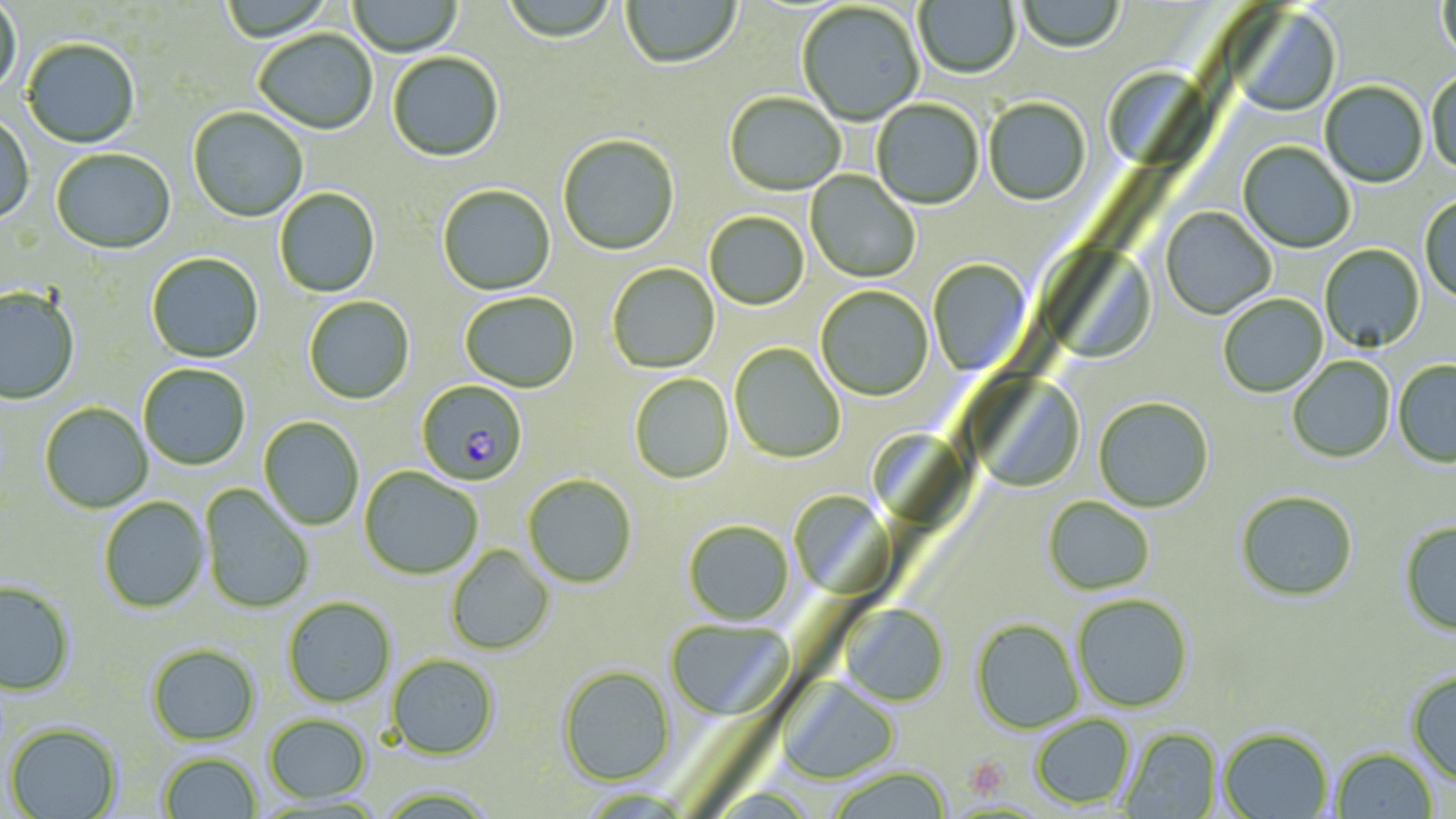

Summary:
  - Coordinate format: approximate bounding boxes as (x1,y1)-(x2,y2) corner pairs in pixels
  - Plasmodium falciparum-infected red blood cell locations: (415,380)-(528,487)
  - Uninfected red blood cell locations: (219,0)-(336,44), (500,0)-(619,46), (621,0)-(742,72), (914,0)-(1020,80), (1017,0)-(1124,54), (1438,0)-(1456,65), (0,1)-(21,101), (347,1)-(463,58), (797,4)-(924,127), (1232,8)-(1342,118), (253,31)-(377,137), (22,40)-(140,150), (387,54)-(504,164), (1103,57)-(1227,175), (1426,69)-(1456,177), (1320,81)-(1428,189), (724,94)-(845,197), (983,98)-(1091,207), (872,99)-(984,210), (188,108)-(308,223), (0,114)-(34,226), (557,136)-(680,257), (1238,142)-(1355,254), (51,149)-(176,256), (806,171)-(920,283), (437,186)-(556,297), (274,188)-(381,298), (1419,194)-(1456,304), (1160,206)-(1276,320), (704,212)-(809,310), (1319,243)-(1425,353), (1043,244)-(1156,365), (146,253)-(264,364), (928,259)-(1033,376), (607,263)-(720,374), (815,286)-(933,401), (0,288)-(80,406), (459,293)-(579,393), (1218,294)-(1328,398), (304,296)-(415,405), (729,343)-(845,464), (1287,356)-(1395,463), (1393,360)-(1456,468), (138,364)-(250,471), (966,373)-(1086,494), (629,374)-(734,484), (1093,396)-(1214,512), (39,403)-(153,514), (258,416)-(364,531), (869,434)-(967,530), (359,467)-(482,580), (523,474)-(637,588), (199,484)-(315,615), (789,488)-(896,598), (1235,490)-(1359,601), (98,496)-(210,614), (1043,497)-(1155,595), (683,519)-(794,626), (1399,521)-(1456,636), (446,544)-(554,655), (0,581)-(75,697), (1071,594)-(1193,713), (283,597)-(396,707), (839,604)-(949,707), (970,618)-(1083,733), (665,619)-(793,721), (147,644)-(260,745), (386,653)-(500,760), (557,666)-(676,785), (1405,672)-(1456,786), (777,676)-(899,785), (263,714)-(372,803), (1030,714)-(1135,809), (5,722)-(122,819), (1219,727)-(1333,818), (1119,728)-(1222,818), (1331,747)-(1438,818), (158,752)-(262,818), (825,766)-(953,819), (375,787)-(499,818)
  - Platelet locations: (968,755)-(1011,796)
  - Slide-level diagnosis: Plasmodium falciparum
  - Stain: May-Grünwald-Giemsa
  - Modality: light microscopy
  - Field of view: single
  - Preparation: thin blood smear
  - Magnification: 1000x
  - Image size: 1456×819 pixels